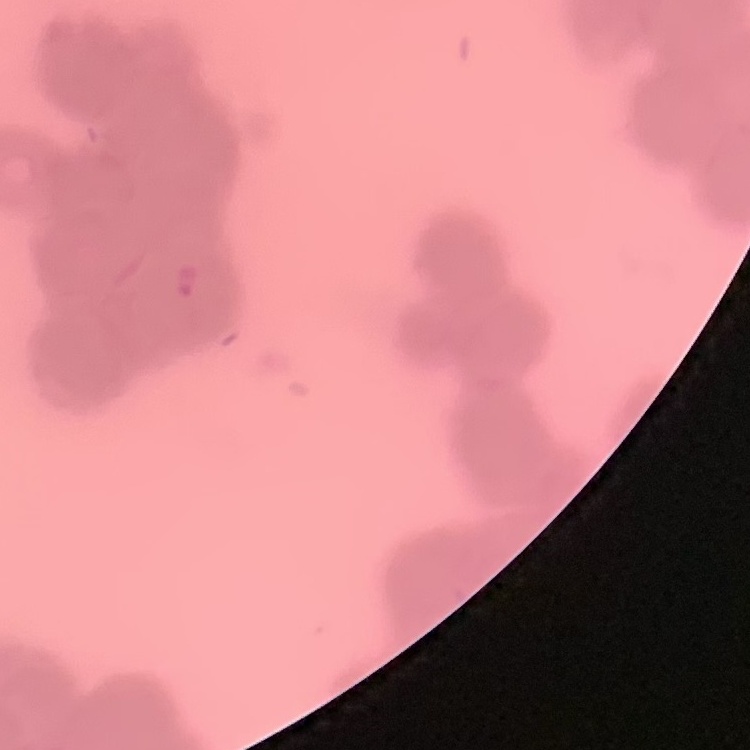

red blood cell morphology = rouleaux formation
stain = Field's or Giemsa
image type = one tile cut from a larger photomicrograph
preparation = thin blood smear